State which parasite is depicted.
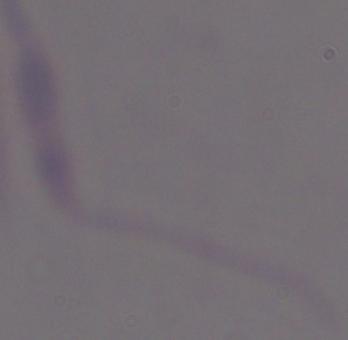
Leishmania.

Captured at 1000x magnification. Micrograph.